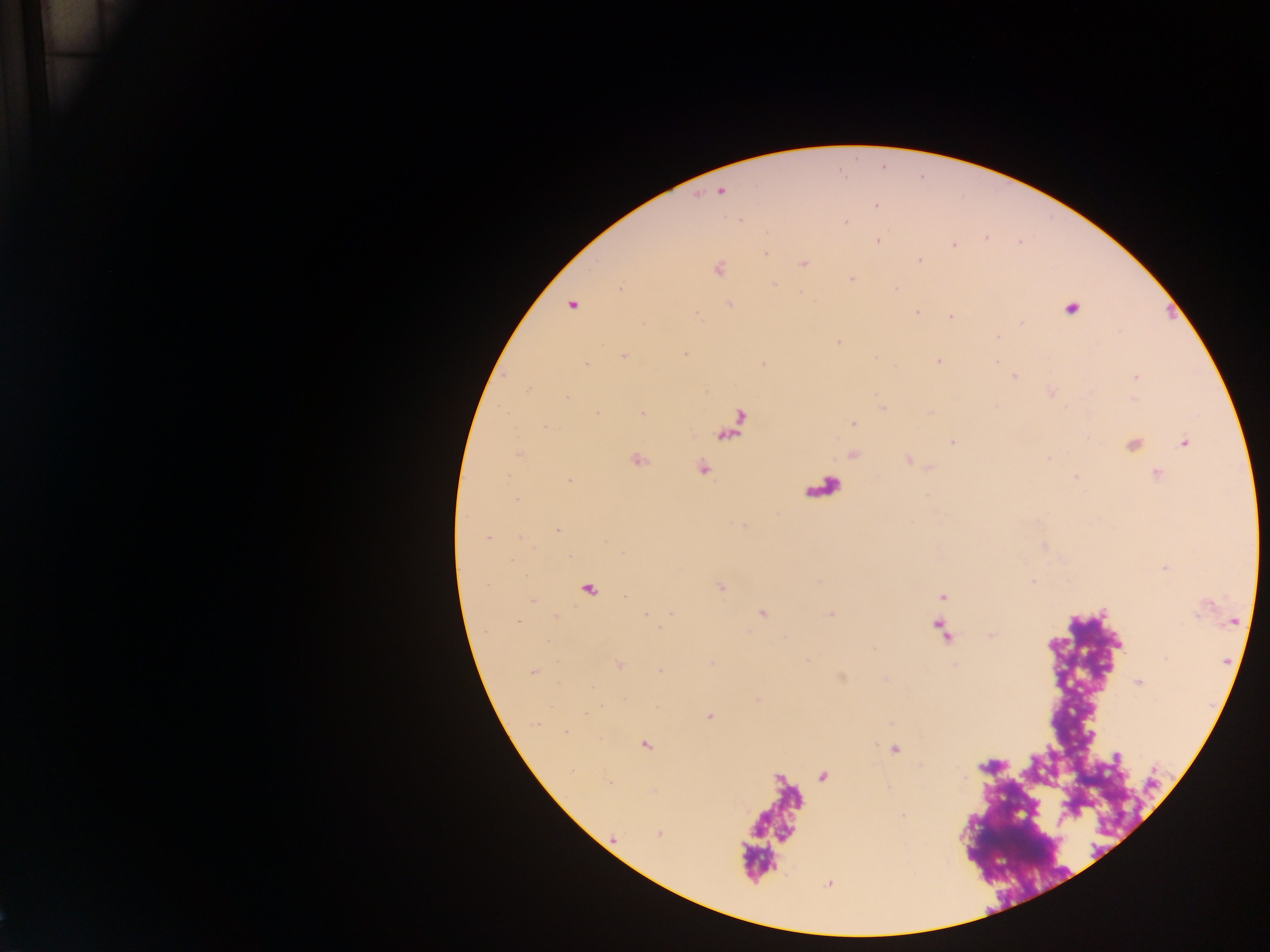

Approximate centers as [x, y] in pixels.
Summary:
  - Plasmodium parasite locations: [721, 192], [876, 205], [845, 222], [986, 238], [878, 240], [954, 246], [765, 253], [920, 260], [804, 263], [718, 269], [852, 278], [774, 285], [896, 288], [729, 304], [572, 306], [1071, 309], [917, 312], [696, 315], [951, 317], [1021, 324], [997, 338], [839, 342], [685, 354], [623, 356], [939, 362], [586, 365], [764, 365], [1014, 376], [1136, 377], [529, 388], [1052, 394], [567, 397], [598, 413], [643, 413], [852, 424], [546, 427], [953, 442], [1185, 443], [1134, 445], [519, 453], [638, 460], [702, 468], [1157, 473], [1076, 477], [569, 481], [517, 499], [557, 530], [488, 539], [720, 588], [942, 596], [532, 601], [671, 612], [762, 613], [517, 621], [619, 665], [534, 672], [1139, 682], [709, 716], [535, 724], [565, 731], [646, 745], [894, 749], [1117, 756], [609, 782], [903, 816], [659, 833], [613, 838]
  - Leukocyte locations: [734, 425]
  - Country: Ghana
  - Image size: 1270×952 pixels
  - Field of view: single
  - Preparation: thick blood smear
  - Capture: mobile-phone photograph through a microscope